State which cell type is depicted.
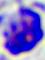

This is a leukocyte.

Photomicrograph. Captured at 400x magnification.